Locate every blood parasite and identify its species.
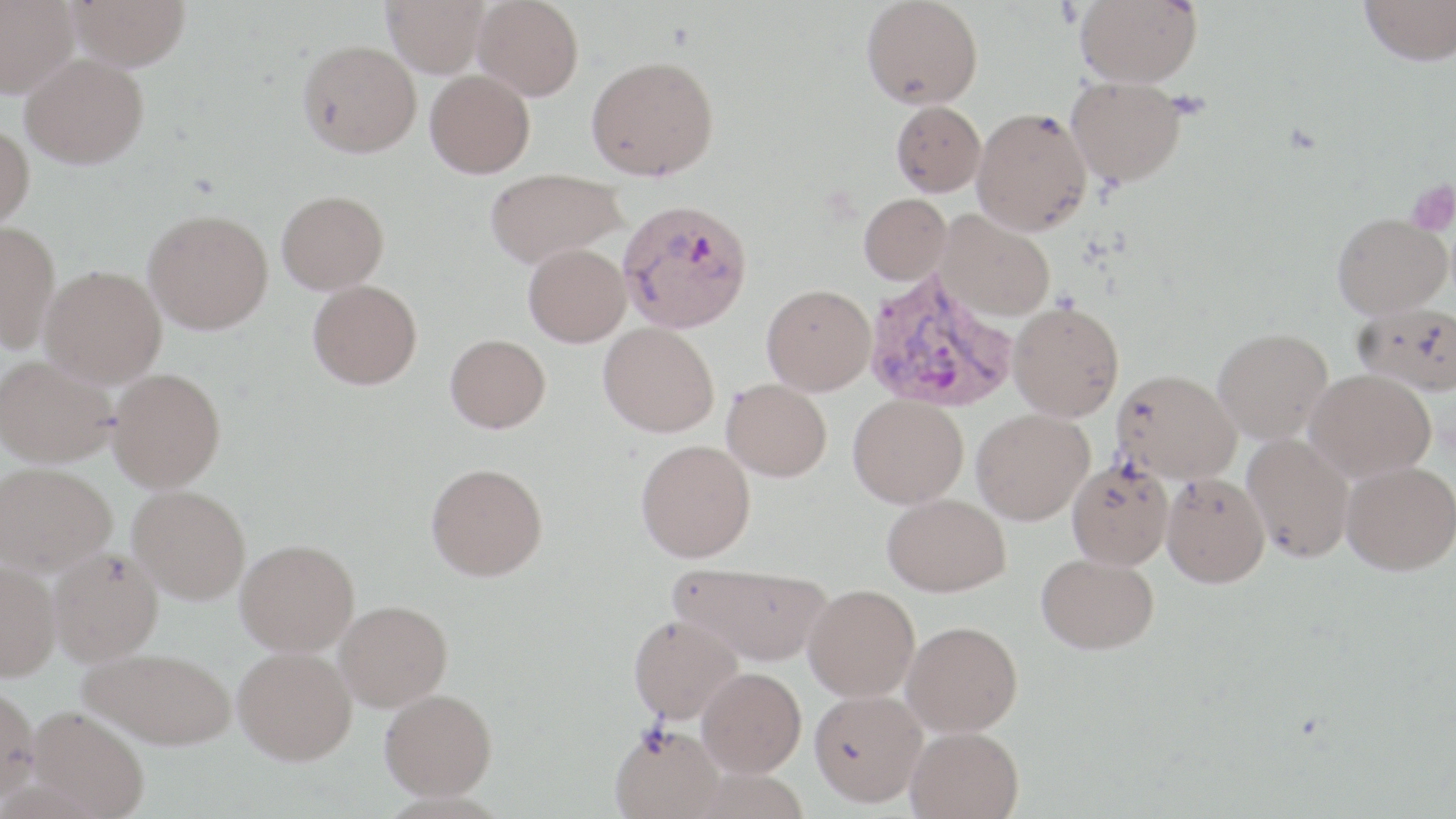
Approximate bounding boxes as (x1,y1)-(x2,y2) corner pairs in pixels.
Plasmodium vivax-infected red blood cells: (618,202)-(754,337), (862,269)-(1018,415).
No Plasmodium falciparum, Plasmodium ovale, Plasmodium malariae, Babesia divergens, or Trypanosoma brucei observed.

Uninfected red blood cell locations: (0,0)-(80,98), (69,0)-(190,71), (382,0)-(489,77), (474,0)-(583,100), (862,0)-(983,111), (1075,0)-(1202,87), (1360,0)-(1456,66), (297,40)-(421,157), (21,53)-(148,168), (586,58)-(720,182), (425,70)-(535,178), (1066,75)-(1186,188), (891,100)-(985,197), (972,107)-(1092,235), (0,123)-(34,231), (487,168)-(626,269), (278,191)-(389,295), (859,194)-(951,286), (937,212)-(1054,321), (144,213)-(273,337), (1331,213)-(1452,318), (0,221)-(59,351), (523,247)-(631,350), (41,265)-(166,386), (308,280)-(422,392), (762,286)-(875,396), (1008,301)-(1124,422), (1354,302)-(1456,395), (598,324)-(719,439), (1213,328)-(1333,444), (445,336)-(551,436), (0,355)-(116,467), (1305,368)-(1436,482), (108,369)-(226,492), (1113,369)-(1241,482), (722,379)-(832,482), (848,394)-(968,509), (971,409)-(1094,525), (1242,432)-(1354,562), (637,440)-(757,564), (1066,458)-(1174,570), (1341,461)-(1456,575), (0,462)-(116,574), (426,466)-(548,585), (1161,472)-(1269,587), (129,487)-(250,605), (883,493)-(1010,597), (235,542)-(360,661), (49,546)-(163,665), (1036,553)-(1158,654), (0,561)-(60,680), (672,566)-(832,667), (804,584)-(920,702), (336,602)-(453,712), (629,615)-(743,723), (903,622)-(1023,737), (82,648)-(235,749), (234,648)-(357,765), (697,668)-(806,777), (0,684)-(40,802), (380,689)-(497,800), (809,690)-(926,808), (27,707)-(150,818), (612,724)-(724,819), (905,726)-(1024,819). Platelet locations: (1406,180)-(1456,235). Slide-level diagnosis: Plasmodium vivax. Light microscopy. Image is 1456×819 pixels. Single field of view. Thin blood film. Captured at 1000x magnification. May-Grünwald-Giemsa-stained preparation.